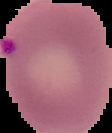

preparation = thin blood smear
result = Plasmodium parasites detected
image type = segmented cell region with the area outside set to black
image size = 112×133 pixels